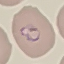
Summary:
  - Malaria status: parasitized
  - Capture: smartphone through the microscope eyepiece
  - Image type: automatically extracted cell patch, resized to 64 × 64 pixels
  - Stain: Giemsa
  - Preparation: thin blood smear